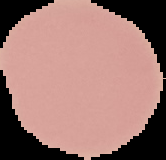
preparation = thin blood smear
image size = 166×160 pixels
result = no Plasmodium parasites seen
image type = segmented cell region on a black background